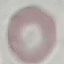

Summary:
  - Result: negative for malaria parasites
  - Capture: smartphone through the microscope eyepiece
  - Stain: Giemsa
  - Preparation: thin smear
  - Image type: automatically extracted cell patch, resized to 64 × 64 pixels